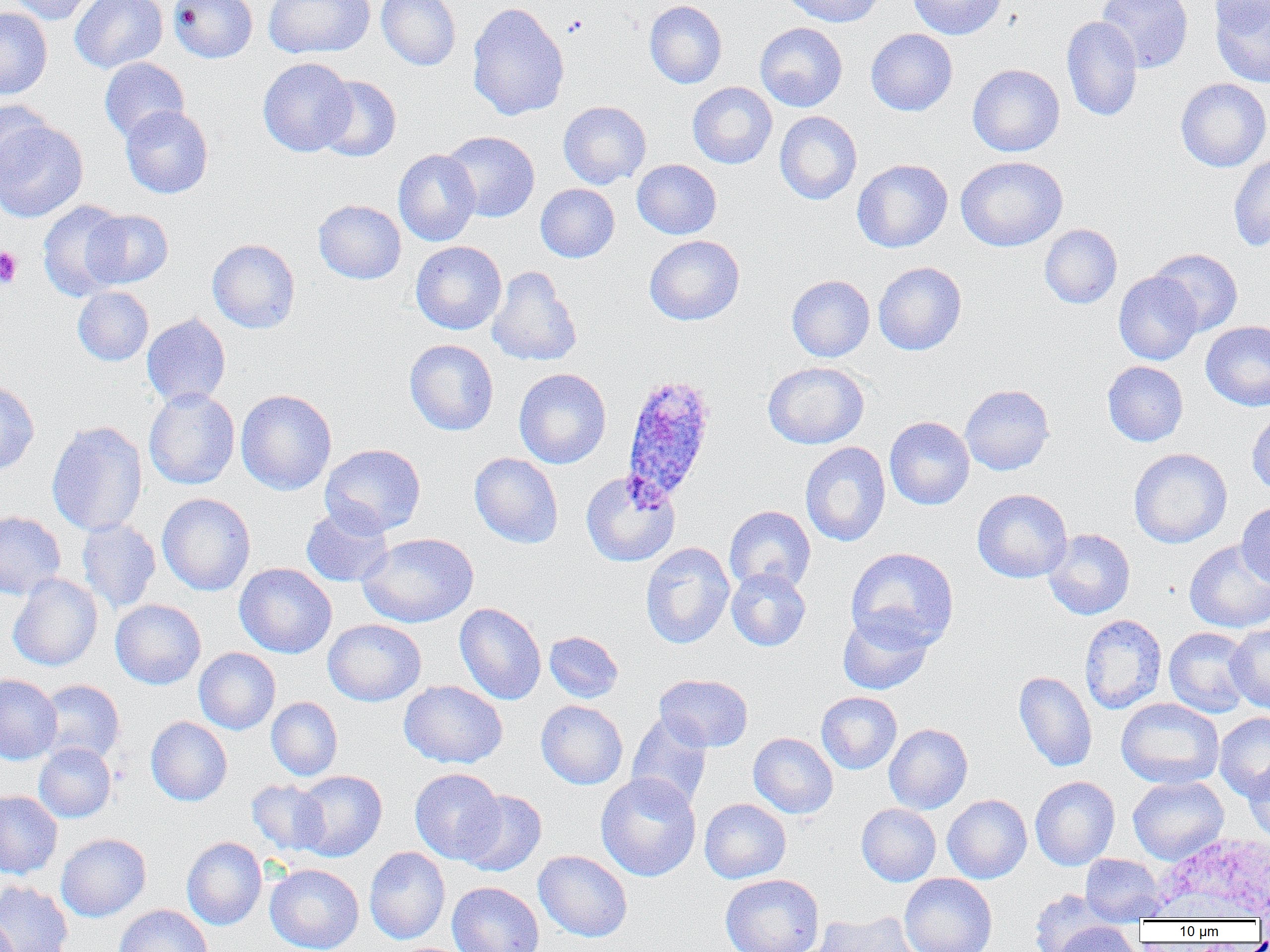

Plasmodium ovale-infected red blood cell locations = approximate bounding boxes as (x1, y1, x2, y2) in pixels: (620, 373, 717, 504)
slide-level diagnosis = Plasmodium ovale
modality = light microscopy
magnification = 1000x
field of view = one of a larger specimen
preparation = thin blood smear
platelet locations = approximate bounding boxes as (x1, y1, x2, y2) in pixels: (0, 246, 23, 289)
uninfected red blood cell locations (subset) = approximate bounding boxes as (x1, y1, x2, y2) in pixels: (8, 0, 101, 25), (70, 0, 168, 73), (168, 0, 257, 63), (263, 0, 375, 59), (376, 0, 461, 71), (784, 0, 884, 27), (907, 0, 1007, 40), (1096, 0, 1193, 73), (1209, 0, 1270, 35), (644, 1, 727, 88), (1209, 1, 1270, 88), (467, 2, 569, 121), (0, 7, 52, 99), (1061, 15, 1143, 122), (755, 22, 848, 112), (866, 29, 957, 116), (99, 57, 189, 143), (258, 57, 356, 157), (967, 63, 1065, 156), (315, 76, 401, 162), (1175, 78, 1270, 171), (687, 82, 777, 169), (0, 100, 53, 190), (558, 101, 651, 188), (120, 105, 214, 198), (774, 111, 862, 205), (0, 118, 89, 222), (442, 131, 540, 222), (393, 149, 481, 246), (1228, 151, 1270, 252), (956, 156, 1068, 251), (632, 159, 721, 239), (852, 159, 953, 252), (535, 184, 620, 262), (313, 199, 406, 284), (37, 200, 129, 301), (85, 210, 174, 289), (1040, 224, 1122, 309), (644, 235, 745, 325), (207, 239, 300, 333), (410, 241, 506, 334), (1148, 248, 1243, 336), (873, 261, 967, 355), (487, 266, 582, 367), (1113, 271, 1203, 365), (786, 275, 875, 362), (72, 286, 154, 366), (142, 313, 231, 408), (1201, 320, 1270, 411), (405, 339, 498, 436), (763, 361, 869, 449), (1102, 361, 1188, 446), (513, 368, 611, 469), (0, 381, 40, 476), (960, 384, 1054, 475), (144, 387, 240, 489), (236, 389, 337, 495), (1246, 410, 1270, 496), (884, 416, 975, 510), (46, 420, 148, 537), (799, 442, 890, 547), (320, 444, 426, 537), (1128, 448, 1232, 548), (469, 453, 564, 548), (580, 470, 680, 566), (972, 488, 1072, 583), (156, 493, 255, 596), (1236, 501, 1270, 588), (301, 505, 393, 587), (724, 505, 816, 593), (0, 511, 65, 599), (77, 518, 161, 613), (1043, 528, 1135, 620), (358, 532, 479, 628), (1184, 540, 1270, 633), (640, 542, 735, 649), (845, 547, 959, 652), (234, 563, 337, 658), (727, 567, 811, 651), (8, 573, 103, 671), (110, 599, 206, 689), (454, 602, 546, 705), (838, 609, 934, 695), (1079, 614, 1167, 714), (323, 619, 426, 706), (1225, 623, 1270, 713), (1164, 627, 1253, 718), (544, 631, 624, 703), (194, 647, 280, 735), (1013, 670, 1097, 772), (0, 674, 62, 764), (654, 674, 753, 752), (36, 679, 125, 765), (400, 680, 508, 768), (816, 692, 902, 774), (266, 697, 343, 781), (1116, 697, 1224, 789), (536, 700, 628, 789), (626, 712, 713, 811), (1214, 712, 1270, 801), (146, 716, 232, 806), (884, 723, 973, 814), (748, 732, 838, 819), (34, 743, 116, 822), (1245, 758, 1270, 842), (409, 768, 504, 864), (293, 770, 387, 862), (596, 772, 701, 881), (1030, 776, 1120, 870), (1127, 776, 1228, 864), (247, 780, 330, 855), (0, 790, 62, 879), (456, 790, 546, 877), (943, 794, 1032, 883), (700, 798, 791, 883), (856, 803, 941, 886), (56, 833, 151, 922), (182, 837, 267, 930), (364, 846, 450, 945), (533, 850, 632, 942), (1080, 853, 1168, 925), (265, 863, 364, 952), (899, 873, 997, 952), (720, 874, 824, 952), (0, 881, 73, 952), (447, 881, 544, 952), (1028, 889, 1113, 952), (114, 905, 213, 952), (0, 907, 18, 952), (811, 911, 922, 952), (1051, 921, 1141, 952)
image size = 1270×952 pixels